State which parasite is depicted.
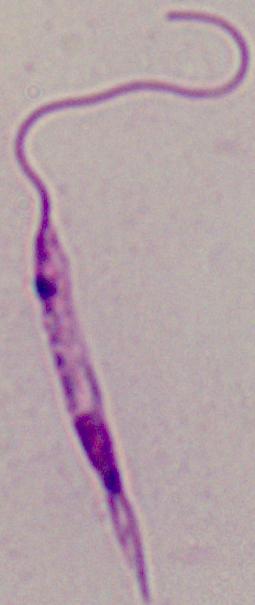

Leishmania.

Summary:
  - Modality: micrograph
  - Magnification: 1000x